Name the parasite shown.
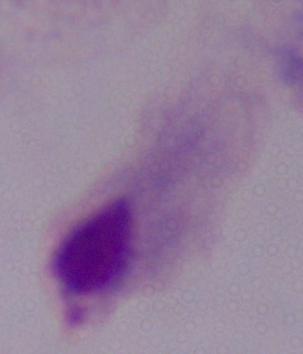

This is a trichomonad.

Summary:
  - Magnification: 1000x
  - Modality: photomicrograph